Locate and identify every blood parasite.
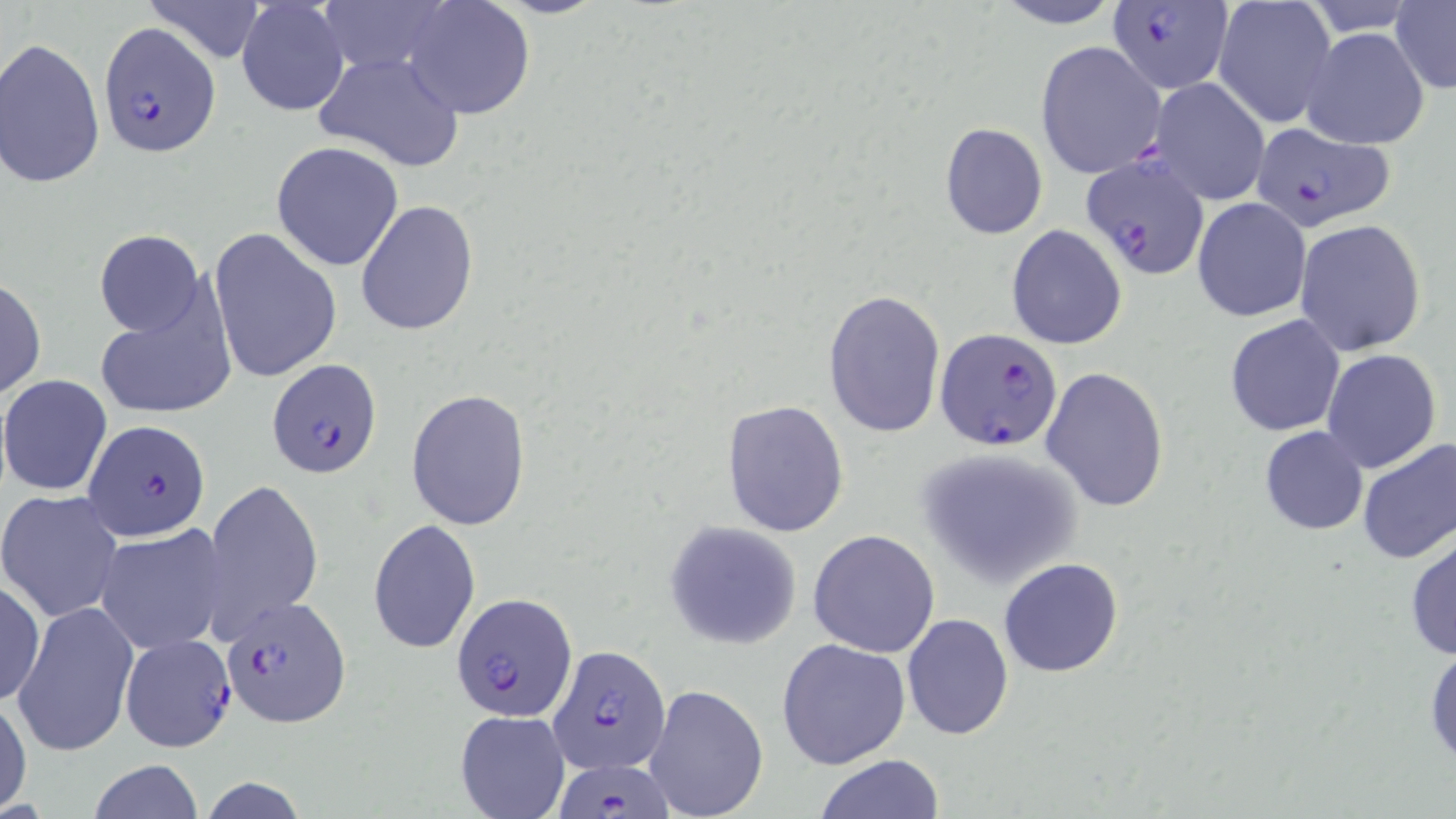

Approximate bounding boxes as (x1, y1, x2, y2) in pixels.
Plasmodium falciparum-infected red blood cells: (1105, 0, 1235, 95), (97, 24, 219, 157), (1248, 122, 1396, 233), (1082, 156, 1212, 280), (934, 327, 1061, 450), (268, 361, 383, 480), (83, 417, 211, 542), (450, 591, 580, 724), (222, 598, 351, 728), (117, 630, 236, 754), (542, 648, 670, 774), (552, 755, 676, 818).
No Plasmodium ovale, Plasmodium malariae, Plasmodium vivax, Babesia divergens, or Trypanosoma brucei observed.

Uninfected red blood cell locations: (139, 0, 272, 65), (236, 0, 350, 118), (990, 0, 1127, 29), (1213, 0, 1337, 128), (1390, 1, 1456, 92), (401, 2, 535, 121), (1301, 26, 1430, 149), (1, 36, 106, 190), (1035, 39, 1166, 179), (312, 51, 466, 173), (1147, 77, 1271, 206), (940, 122, 1048, 240), (271, 141, 404, 270), (1192, 198, 1311, 322), (356, 200, 479, 336), (1294, 219, 1426, 356), (1006, 225, 1126, 349), (208, 227, 342, 383), (94, 230, 204, 337), (0, 274, 46, 401), (823, 287, 946, 438), (93, 288, 238, 424), (1225, 314, 1346, 437), (1320, 348, 1442, 474), (1040, 365, 1170, 512), (1, 374, 114, 496), (405, 389, 531, 530), (721, 399, 851, 539), (1259, 425, 1370, 535), (1356, 437, 1456, 564), (915, 447, 1082, 587), (202, 476, 324, 641), (0, 489, 125, 623), (368, 519, 481, 654), (664, 520, 803, 650), (94, 524, 230, 654), (807, 530, 941, 656), (1405, 530, 1456, 661), (998, 558, 1124, 677), (0, 578, 45, 706), (13, 601, 139, 757), (901, 614, 1014, 739), (776, 638, 911, 770), (1425, 643, 1456, 771), (643, 683, 769, 819), (0, 693, 31, 815), (455, 711, 569, 819), (814, 754, 946, 819), (86, 760, 205, 819). Slide-level diagnosis: Plasmodium falciparum. Thin blood smear. One field of a larger specimen. Captured at 1000x magnification. Image is 1456×819 pixels. May-Grünwald-Giemsa stain. Optical microscopy.